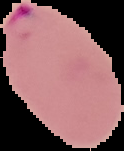

Image is 124×151 pixels. From a thin blood smear. Malaria status: parasitized. Cell region segmented out of the field of view; the surrounding area is masked to black.